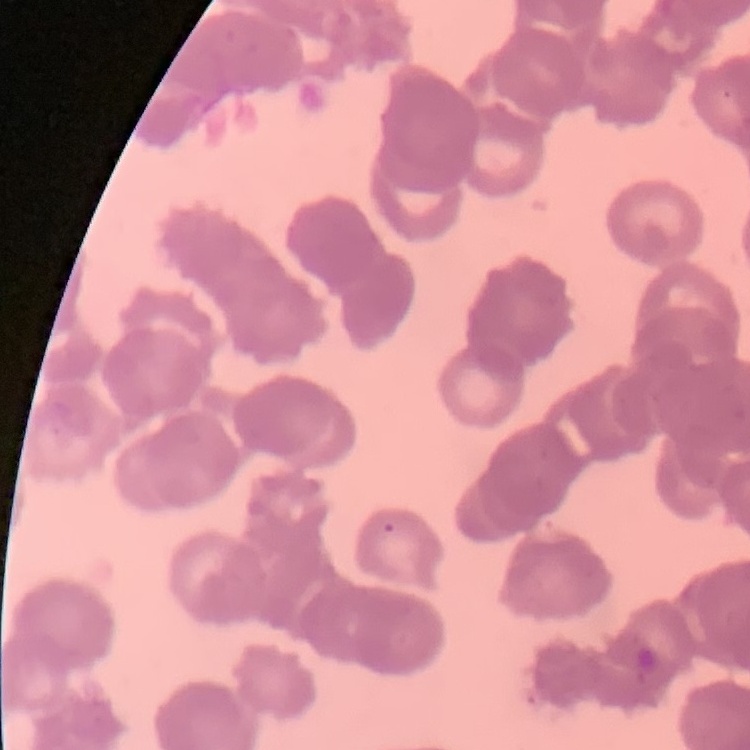
erythrocyte morphology = rouleaux formation
image type = one tile cut from a larger photomicrograph
preparation = thin blood smear
stain = Field's or Giemsa